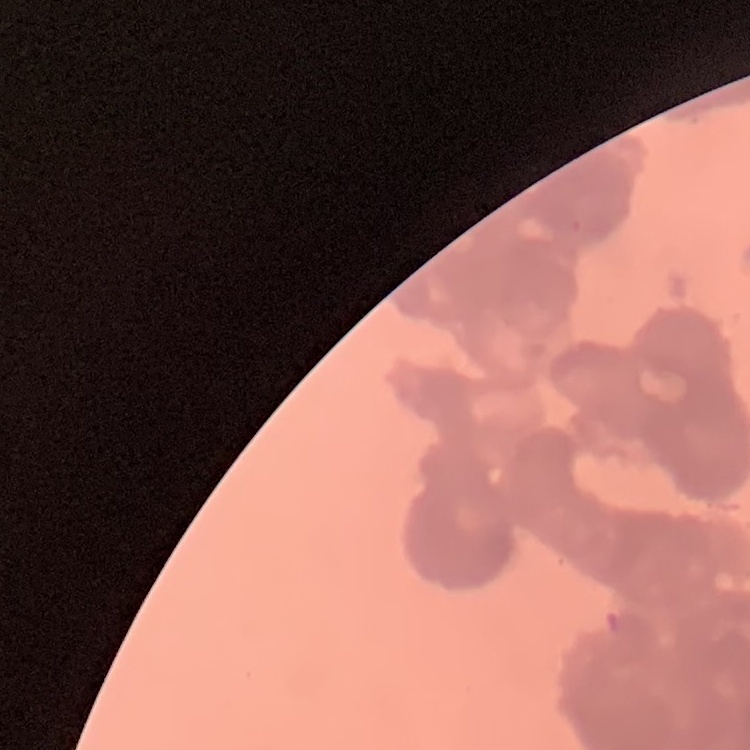
erythrocyte morphology = rouleaux formation
preparation = thin blood smear
stain = Field's or Giemsa
image type = square crop of a larger photomicrograph